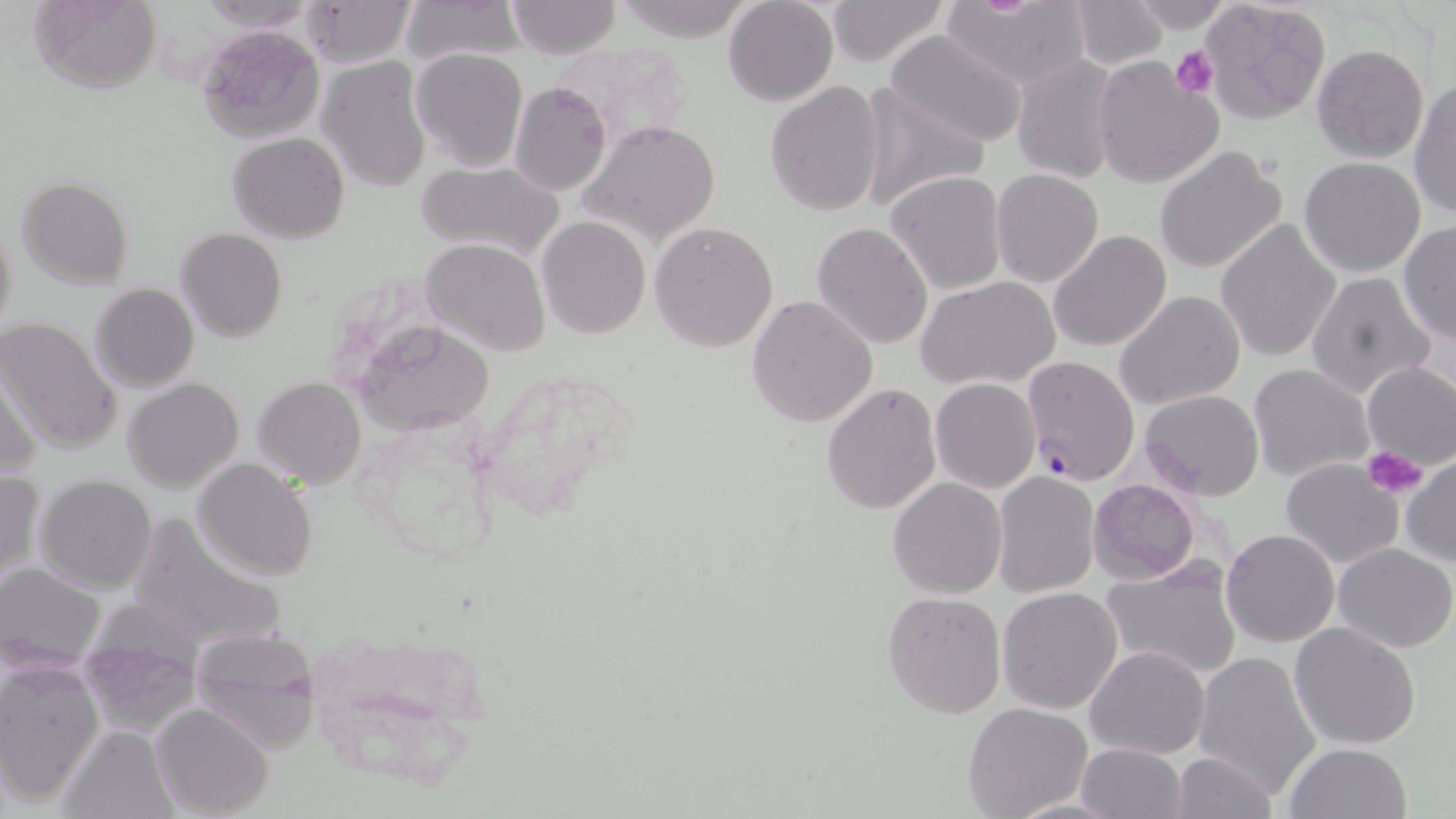

Plasmodium falciparum-infected red blood cell locations = approximate bounding boxes as (x1, y1, x2, y2) in pixels: (1021, 354, 1140, 485)
slide-level diagnosis = Plasmodium falciparum
stain = May-Grünwald-Giemsa
image size = 1456×819 pixels
platelet locations = approximate bounding boxes as (x1, y1, x2, y2) in pixels: (1171, 47, 1221, 100), (1360, 447, 1429, 499)
magnification = 1000x
uninfected red blood cell locations = approximate bounding boxes as (x1, y1, x2, y2) in pixels: (28, 0, 160, 93), (293, 0, 416, 67), (399, 0, 523, 66), (506, 0, 621, 59), (723, 0, 839, 106), (825, 0, 948, 66), (193, 1, 317, 34), (610, 1, 757, 43), (1067, 1, 1169, 69), (1201, 1, 1331, 123), (942, 2, 1093, 92), (1125, 2, 1241, 34), (195, 23, 326, 145), (883, 31, 1031, 149), (552, 40, 695, 149), (1311, 44, 1429, 164), (409, 47, 527, 174), (1010, 53, 1123, 185), (1093, 56, 1226, 190), (317, 57, 432, 193), (1408, 78, 1456, 218), (764, 81, 886, 217), (856, 81, 988, 212), (508, 82, 613, 198), (577, 119, 722, 247), (226, 133, 349, 243), (1154, 146, 1288, 275), (1299, 157, 1427, 278), (417, 161, 566, 261), (990, 169, 1105, 290), (884, 170, 1006, 296), (16, 176, 133, 289), (1, 216, 18, 345), (1214, 216, 1343, 364), (536, 217, 651, 338), (650, 222, 779, 353), (810, 222, 933, 350), (1397, 222, 1455, 343), (175, 228, 288, 345), (1048, 229, 1172, 352), (421, 236, 551, 356), (1304, 272, 1437, 398), (916, 275, 1062, 391), (89, 283, 198, 393), (1115, 289, 1246, 412), (746, 295, 878, 428), (0, 317, 122, 452), (353, 319, 497, 435), (1, 358, 46, 482), (1359, 361, 1456, 473), (1247, 364, 1375, 483), (252, 376, 366, 489), (123, 378, 244, 494), (931, 378, 1042, 493), (822, 383, 943, 514), (1139, 388, 1266, 500), (1399, 454, 1456, 567), (190, 457, 319, 581), (1279, 457, 1407, 570), (0, 469, 44, 585), (992, 471, 1101, 598), (33, 475, 158, 595), (888, 477, 1008, 599), (1088, 478, 1200, 584), (121, 511, 286, 652), (1221, 528, 1341, 647), (1332, 542, 1456, 652), (1099, 559, 1243, 680), (1, 565, 105, 670), (996, 587, 1123, 715), (880, 590, 1007, 720), (77, 621, 201, 737), (1288, 622, 1422, 752), (188, 626, 323, 753), (1085, 645, 1211, 759), (1193, 650, 1323, 801), (1, 661, 103, 805), (151, 702, 275, 818), (963, 702, 1094, 819), (59, 725, 180, 819), (1076, 743, 1189, 819), (1282, 743, 1414, 819), (1169, 751, 1277, 818), (1006, 796, 1131, 817)
field of view = one of a larger specimen
modality = light microscopy
preparation = thin blood smear